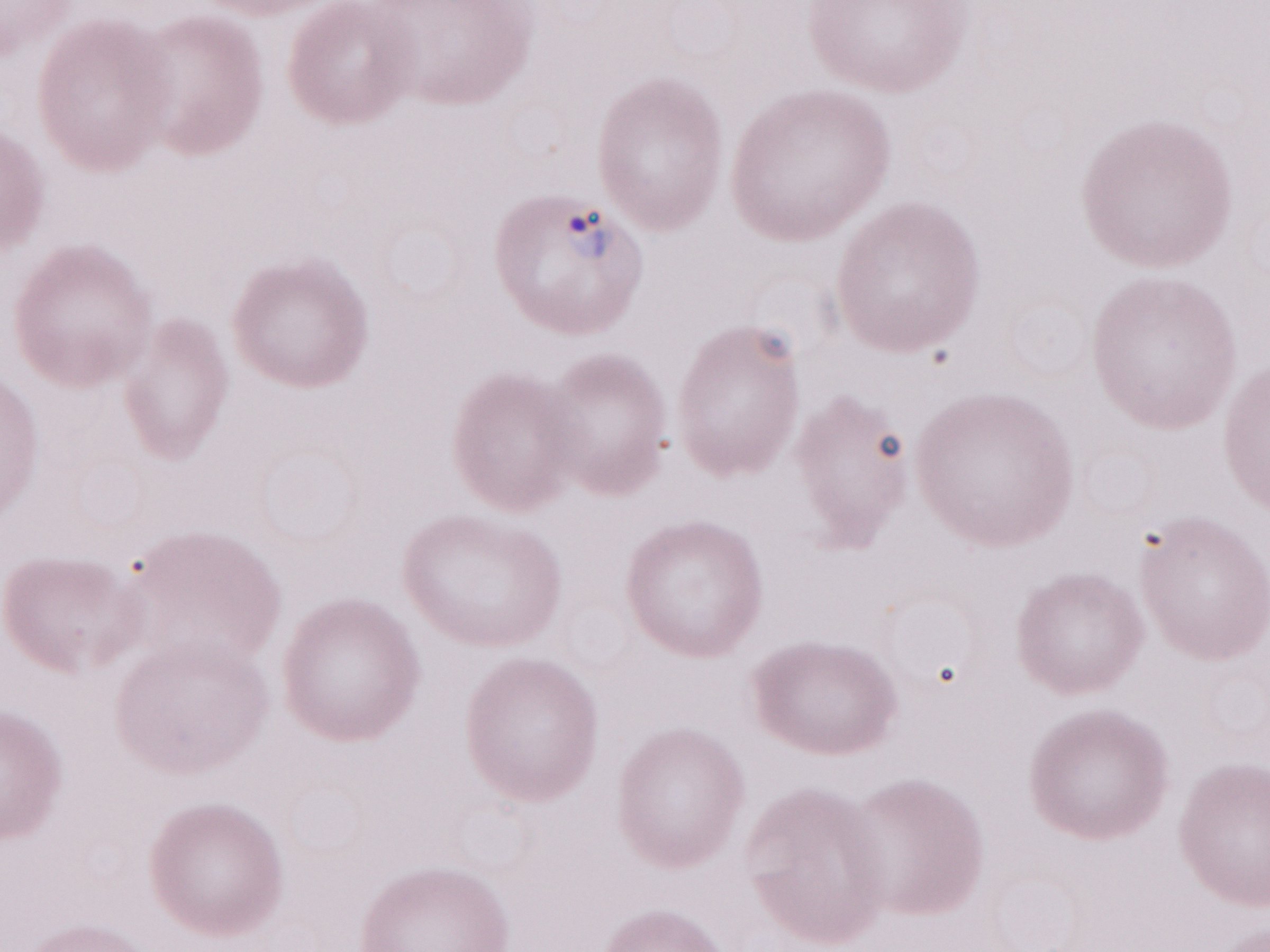

Thin blood film. One field of this slide. Patient diagnosis: malaria infection. 1,000x magnification. Image is 1270×952 pixels. Olympus BX43 microscope, Olympus DP73 camera. May-Grünwald-Giemsa-stained preparation.